Assess this cell for malaria.
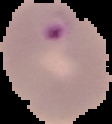

It is parasitized.

Summary:
  - Image size: 112×124 pixels
  - Preparation: thin blood smear
  - Image type: segmented cell region on a black background